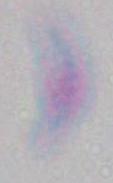

Summary:
  - Magnification: 1000x
  - Identification: Toxoplasma gondii
  - Modality: photomicrograph